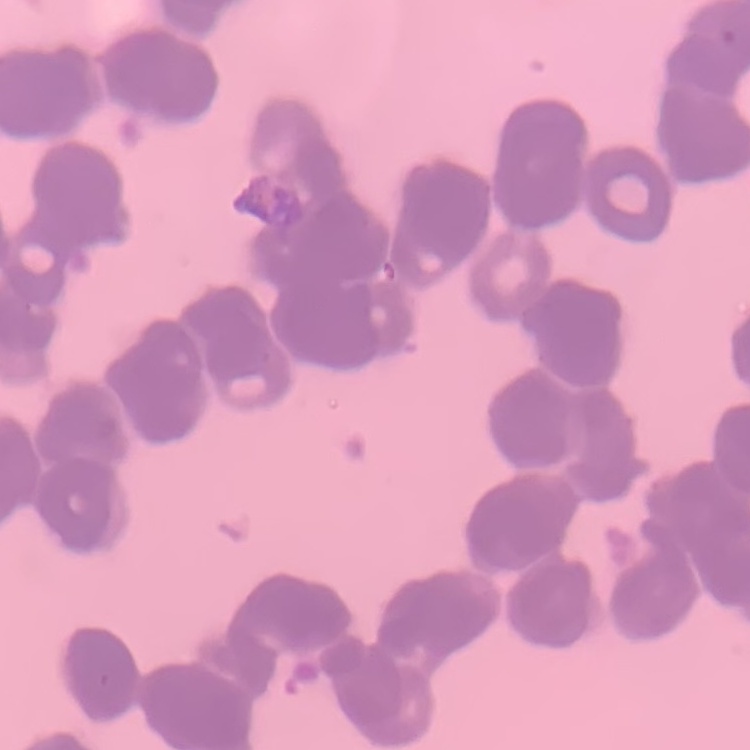
red blood cell morphology = rouleaux formation
preparation = thin blood smear
image type = one tile cut from a larger photomicrograph
stain = Field's or Giemsa